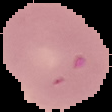
Malaria status: uninfected. From a thin blood film. The area outside the segmented cell region is set to black. Image is 112×112 pixels.